Locate and identify every blood parasite.
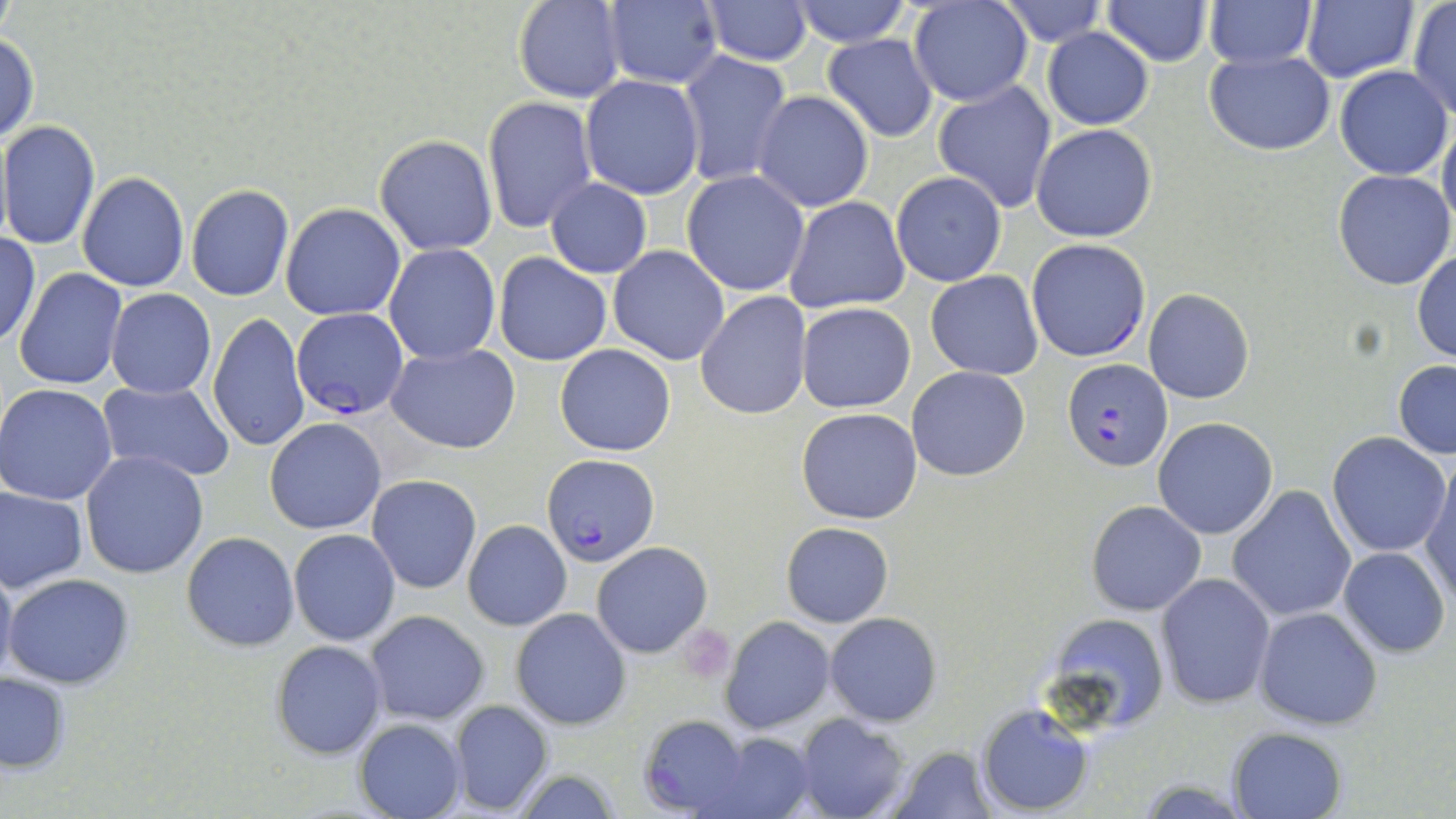

Approximate bounding boxes as [x1, y1, x2, y2] in pixels.
Plasmodium falciparum-infected red blood cells: [1026, 238, 1151, 362], [292, 308, 409, 420], [1062, 361, 1170, 470], [542, 456, 661, 568].
No Plasmodium ovale, Plasmodium malariae, Plasmodium vivax, Babesia divergens, or Trypanosoma brucei observed.

slide-level diagnosis = Plasmodium falciparum
preparation = thin blood film
platelet locations = approximate bounding boxes as [x1, y1, x2, y2] in pixels: [678, 623, 734, 681]
modality = light microscopy
uninfected red blood cell locations = approximate bounding boxes as [x1, y1, x2, y2] in pixels: [604, 0, 724, 90], [788, 0, 913, 48], [998, 0, 1107, 44], [1204, 0, 1316, 68], [1301, 0, 1417, 85], [512, 1, 627, 103], [701, 1, 813, 65], [1102, 1, 1214, 65], [907, 2, 1032, 108], [1406, 2, 1456, 118], [1042, 28, 1154, 129], [0, 29, 38, 145], [821, 34, 938, 142], [676, 50, 792, 186], [1204, 50, 1335, 155], [1334, 65, 1453, 180], [580, 75, 706, 200], [933, 80, 1057, 213], [752, 91, 873, 212], [482, 96, 598, 233], [1438, 114, 1456, 231], [2, 121, 101, 250], [1031, 124, 1158, 243], [374, 134, 498, 256], [682, 170, 811, 296], [1333, 170, 1455, 292], [77, 171, 189, 293], [891, 171, 1006, 286], [545, 179, 652, 277], [185, 184, 294, 302], [783, 196, 910, 314], [280, 204, 405, 320], [0, 230, 41, 348], [384, 243, 502, 365], [607, 246, 730, 365], [1411, 249, 1456, 364], [494, 253, 612, 366], [13, 268, 128, 391], [926, 270, 1044, 381], [105, 288, 216, 398], [1143, 288, 1254, 404], [696, 291, 813, 419], [797, 303, 917, 414], [206, 312, 310, 453], [387, 342, 519, 454], [554, 344, 676, 457], [1392, 360, 1456, 459], [906, 366, 1031, 482], [98, 380, 236, 483], [0, 384, 118, 505], [795, 407, 923, 524], [263, 418, 386, 535], [1152, 419, 1277, 539], [1326, 432, 1450, 557], [80, 449, 209, 579], [1420, 458, 1456, 605], [367, 476, 482, 593], [1228, 485, 1357, 623], [0, 486, 88, 594], [1087, 501, 1206, 615], [462, 520, 571, 630], [781, 522, 892, 627], [288, 529, 401, 645], [181, 531, 299, 652], [591, 541, 712, 658], [1337, 546, 1450, 658], [0, 553, 17, 691], [5, 572, 134, 689], [1156, 573, 1275, 708], [511, 607, 631, 729], [1254, 607, 1383, 731], [364, 610, 489, 725], [824, 612, 942, 726], [1040, 613, 1172, 732], [720, 616, 834, 734], [269, 640, 387, 758], [0, 673, 71, 774], [448, 699, 556, 816], [976, 703, 1094, 815], [795, 713, 910, 819], [637, 715, 756, 818], [354, 718, 465, 818], [1227, 727, 1348, 818], [708, 731, 816, 818], [883, 744, 1000, 818], [509, 771, 626, 818]
stain = May-Grünwald-Giemsa
image size = 1456×819 pixels
field of view = one of a larger specimen
magnification = 1000x